Locate leukocytes (white blood cells).
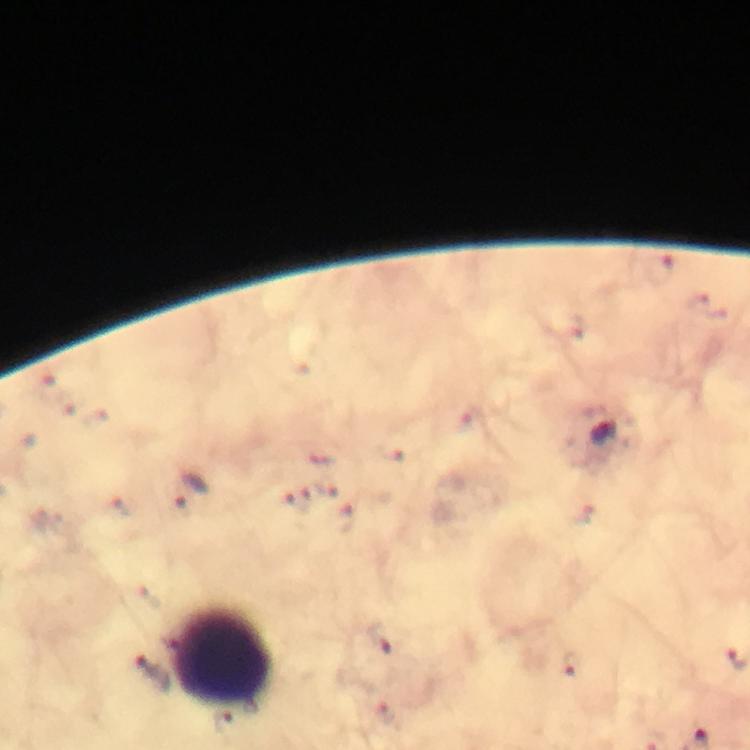

Approximate centers as {x, y} in pixels.
Leukocytes: {221, 659}.

Malaria parasite locations: {662, 269}, {605, 434}, {188, 491}, {297, 497}, {342, 520}, {381, 640}, {571, 665}, {149, 669}. At 100x magnification. Thick smear. From a malaria diagnostic workup. Giemsa stain. Immersion oil applied. Photographed through the microscope with a smartphone camera. A crop from one field of view. Image is 750×750 pixels.